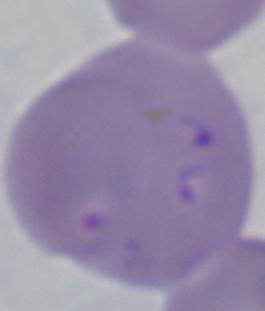
Captured at 1000x magnification. Photomicrograph. A Babesia parasite is seen.